Describe the morphology of the red blood cells.
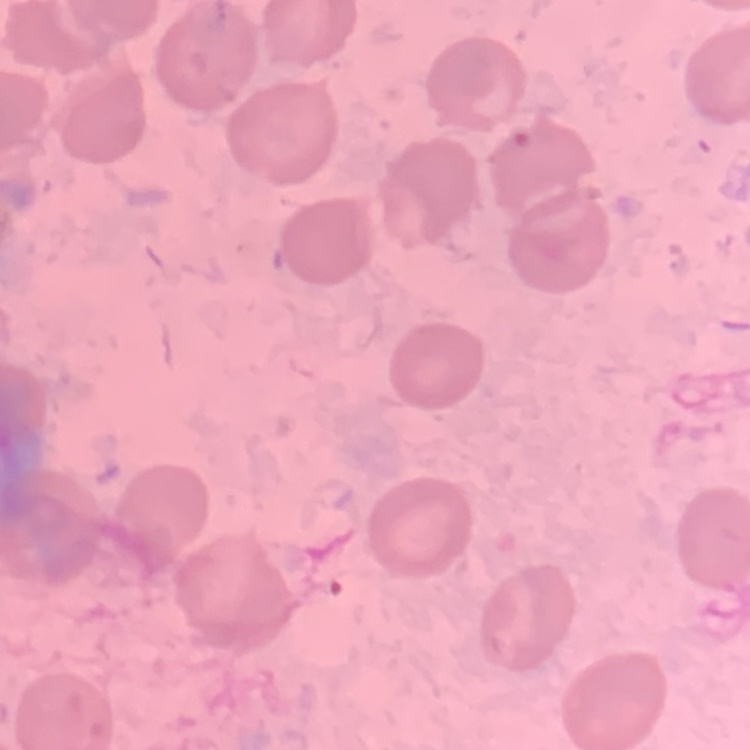
No rouleaux formation.

image_type: square crop of a larger photomicrograph
preparation: thin blood smear
stain: Field's or Giemsa